Describe the morphology of the erythrocytes.
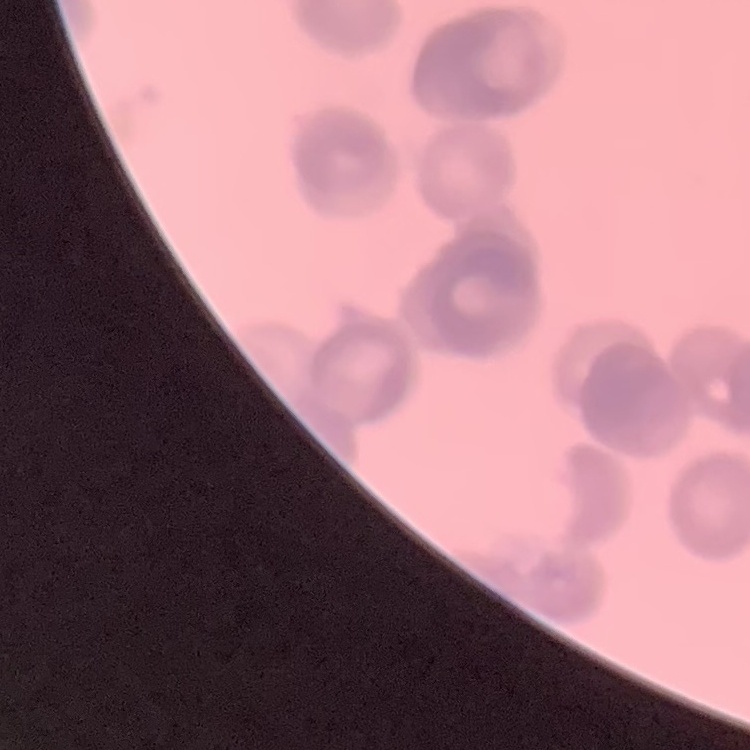
They show rouleaux formation.

{
  "preparation": "thin blood smear",
  "stain": "Field's or Giemsa",
  "image_type": "square crop of a larger photomicrograph"
}